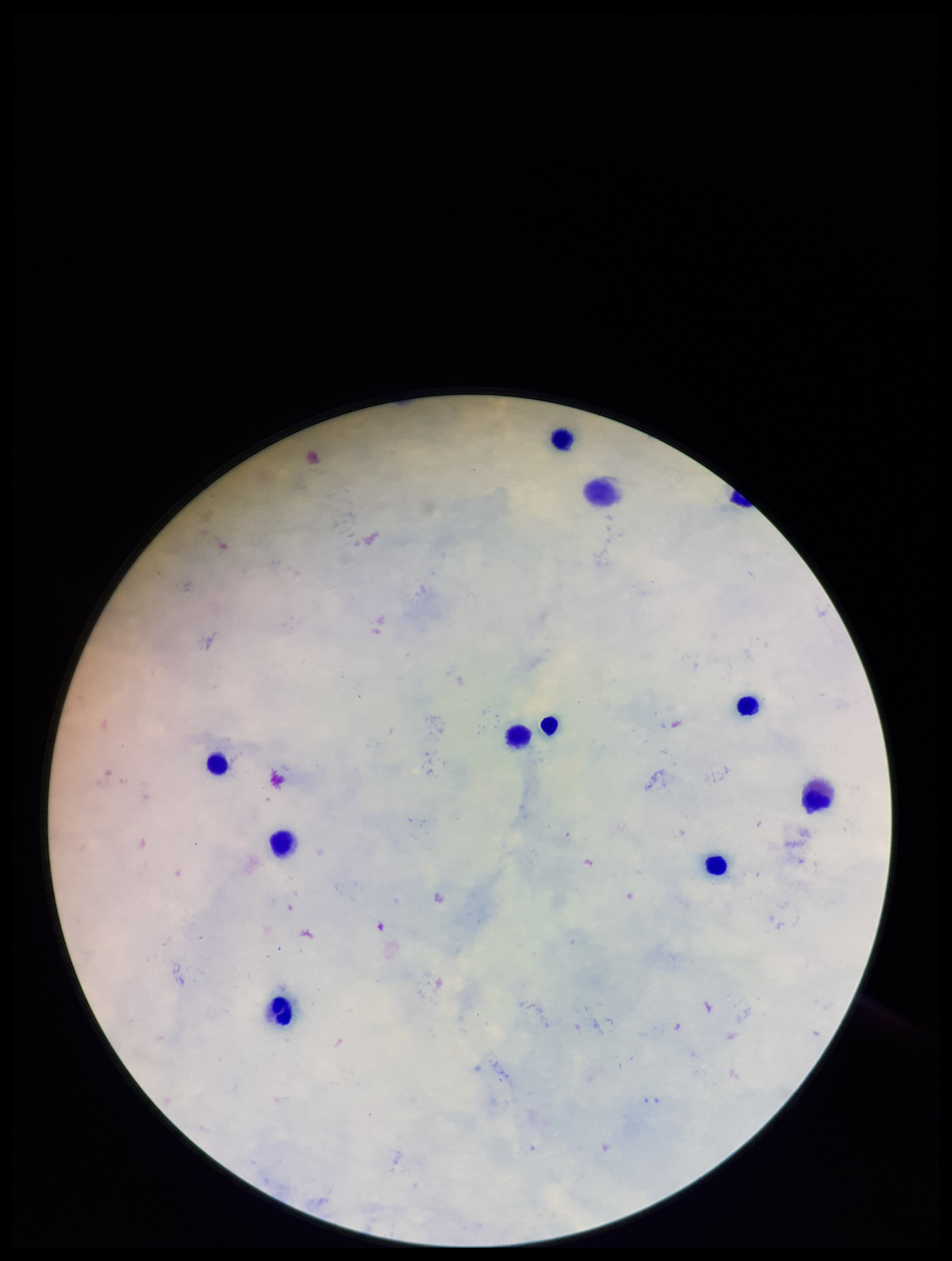 Parasite count: 0. One field from this slide. Image is 952×1261 pixels. Stained with Giemsa. Preparation: thick blood smear. Leukocyte count: 10. Plasmodium parasites: none seen. Patient malaria status: negative. Smartphone photograph taken through the eyepiece of a microscope.